Identify the blood parasite species.
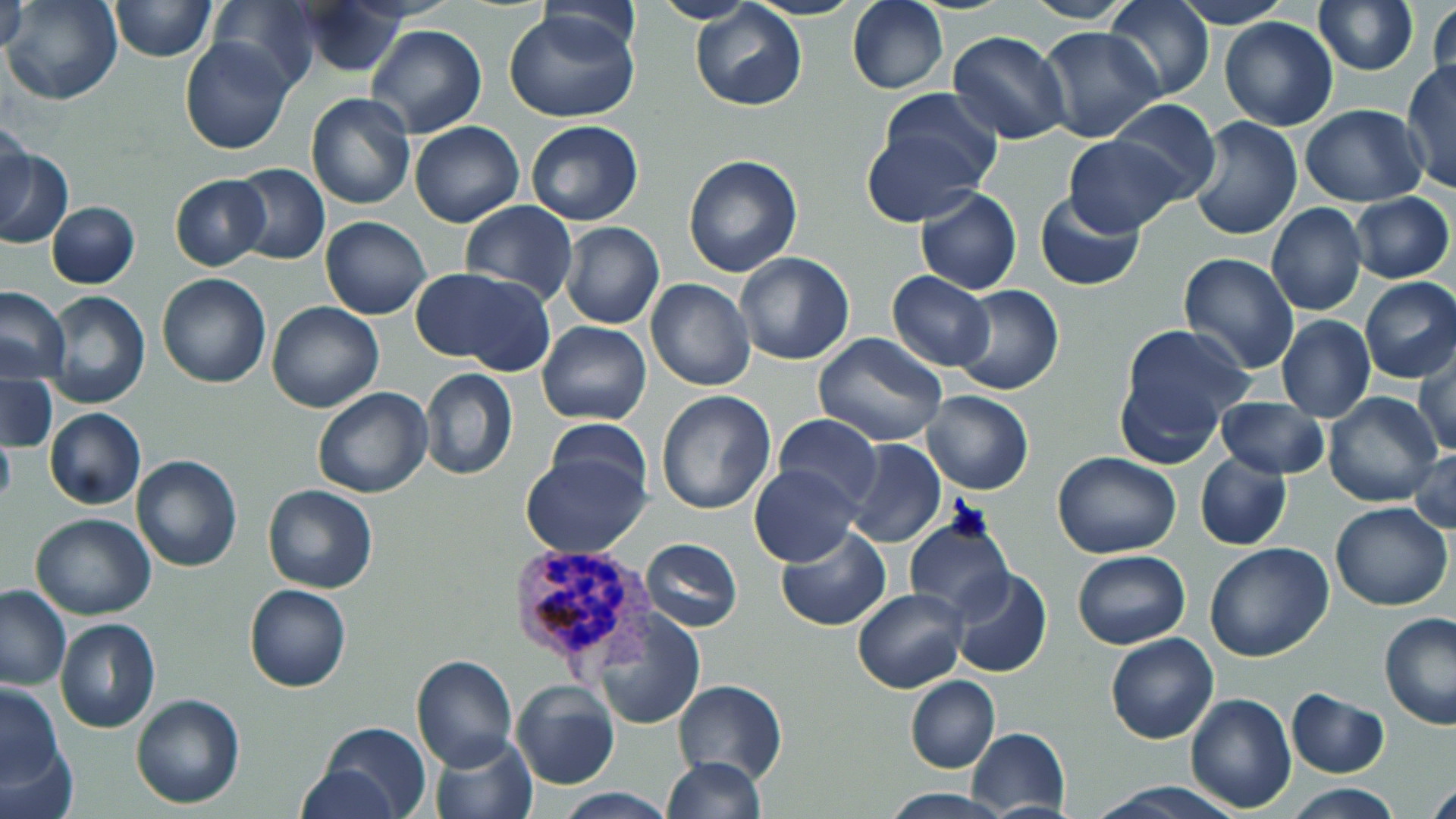

Plasmodium vivax.

uninfected_red_blood_cell_locations: 'approximate bounding boxes as [x1, y1, x2, y2] in pixels: [2, 0, 124, 106], [110, 0, 214, 61], [207, 0, 324, 93], [847, 0, 948, 94], [1105, 0, 1215, 104], [1312, 0, 1419, 76], [1426, 0, 1455, 105], [650, 1, 761, 25], [1019, 1, 1138, 24], [1175, 1, 1291, 29], [2, 3, 28, 52], [296, 3, 409, 77], [690, 3, 808, 110], [503, 8, 643, 125], [1218, 17, 1339, 131], [366, 24, 488, 137], [1037, 26, 1167, 145], [947, 29, 1071, 145], [179, 38, 297, 155], [1401, 61, 1455, 194], [872, 90, 1005, 204], [305, 92, 414, 210], [1107, 98, 1221, 206], [1300, 104, 1425, 205], [0, 115, 33, 222], [1187, 116, 1302, 242], [526, 120, 643, 226], [410, 121, 524, 227], [860, 129, 982, 222], [1063, 134, 1185, 236], [0, 146, 73, 249], [683, 154, 802, 278], [229, 163, 329, 266], [169, 174, 272, 272], [914, 187, 1022, 294], [1036, 190, 1146, 292], [1347, 193, 1453, 284], [460, 199, 577, 303], [47, 201, 140, 289], [1266, 203, 1367, 316], [320, 216, 432, 320], [560, 221, 664, 329], [734, 251, 855, 365], [1177, 252, 1301, 376], [413, 266, 553, 373], [157, 272, 271, 388], [887, 272, 996, 372], [1359, 277, 1456, 384], [646, 278, 755, 391], [951, 285, 1063, 395], [0, 287, 71, 381], [45, 290, 150, 408], [265, 302, 385, 413], [1276, 314, 1376, 423], [537, 321, 652, 426], [1112, 326, 1251, 463], [813, 332, 946, 446], [1414, 346, 1456, 458], [419, 368, 518, 481], [0, 373, 56, 454], [313, 386, 433, 497], [920, 390, 1034, 494], [656, 391, 775, 514], [1322, 392, 1444, 508], [1213, 396, 1332, 479], [44, 408, 146, 510], [775, 415, 882, 512], [0, 420, 16, 518], [538, 422, 654, 511], [843, 439, 947, 550], [1409, 446, 1456, 537], [521, 450, 650, 557], [1052, 452, 1181, 559], [1194, 452, 1291, 551], [133, 455, 242, 572], [749, 463, 864, 568], [262, 484, 378, 594], [1330, 502, 1453, 611], [30, 513, 156, 620], [904, 519, 1011, 623], [776, 526, 890, 631], [642, 537, 744, 632], [1203, 543, 1335, 663], [1072, 549, 1192, 650], [947, 568, 1053, 679], [244, 583, 351, 693], [0, 584, 73, 689], [852, 587, 966, 694], [596, 611, 705, 730], [1379, 613, 1456, 729], [55, 618, 161, 734], [1105, 632, 1218, 744], [410, 654, 518, 770], [905, 675, 1000, 774], [674, 679, 786, 785], [1, 682, 67, 791], [510, 682, 619, 790], [1286, 688, 1389, 778], [1186, 692, 1296, 813], [131, 694, 245, 808], [317, 721, 432, 819], [967, 728, 1070, 814], [0, 730, 78, 819], [429, 732, 537, 818], [660, 757, 764, 819], [297, 762, 400, 818], [1425, 777, 1456, 816], [1088, 781, 1245, 819], [1285, 783, 1402, 818], [880, 788, 1016, 818], [551, 789, 675, 819]'
plasmodium_vivax_infected_red_blood_cell_locations: 'approximate bounding boxes as [x1, y1, x2, y2] in pixels: [507, 543, 653, 676]'
image_size: 1456×819 pixels
modality: optical microscopy
field_of_view: single
magnification: 1000x
preparation: thin blood film
stain: May-Grünwald-Giemsa